Identify the preparation type.
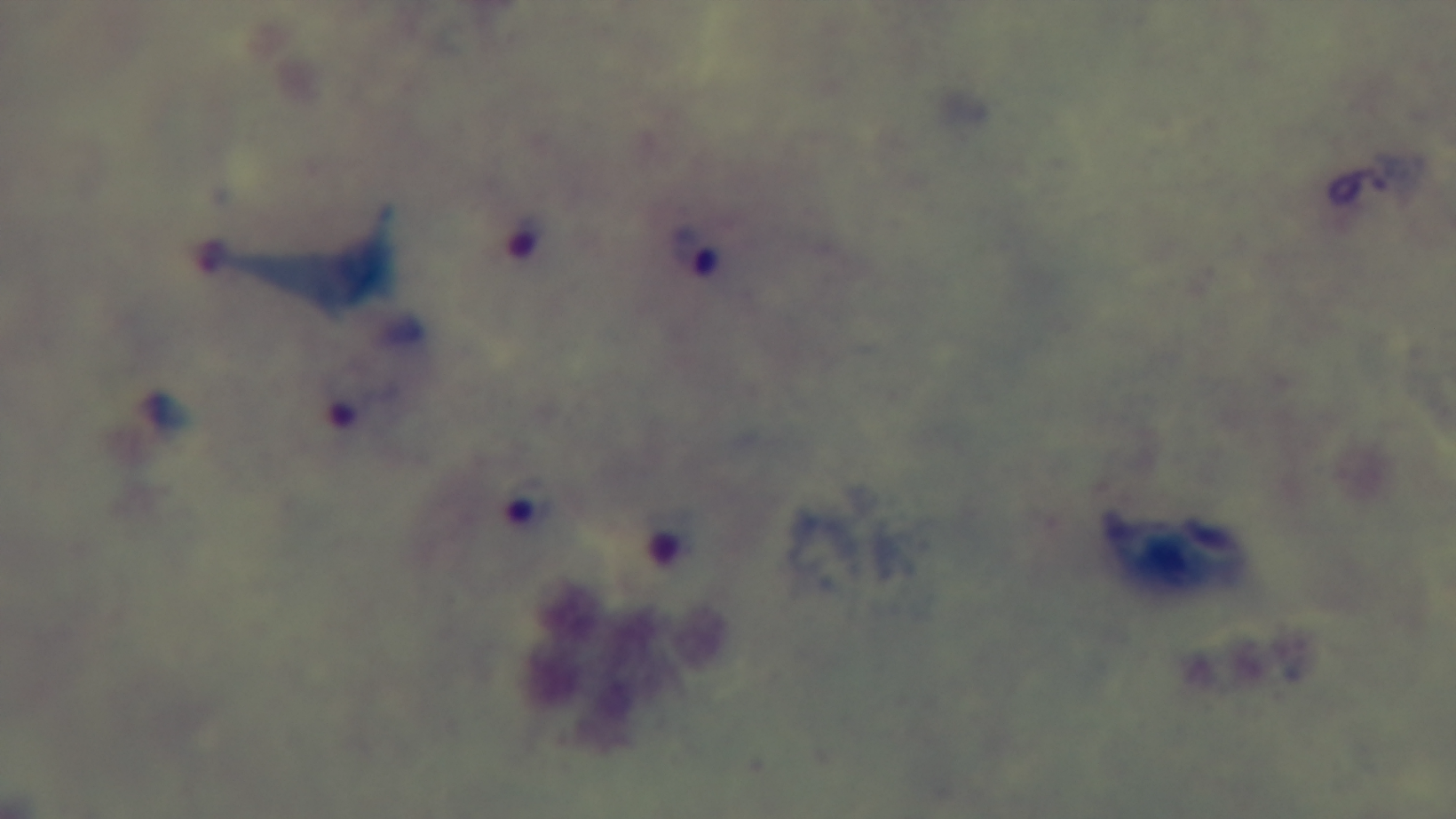

A thick smear.

stain = Giemsa
modality = light microscopy
malaria status = infected
field of view = one from the slide
capture = mounted 4K digital camera
objective = 100x oil immersion